Point out every malaria parasite and every leukocyte.
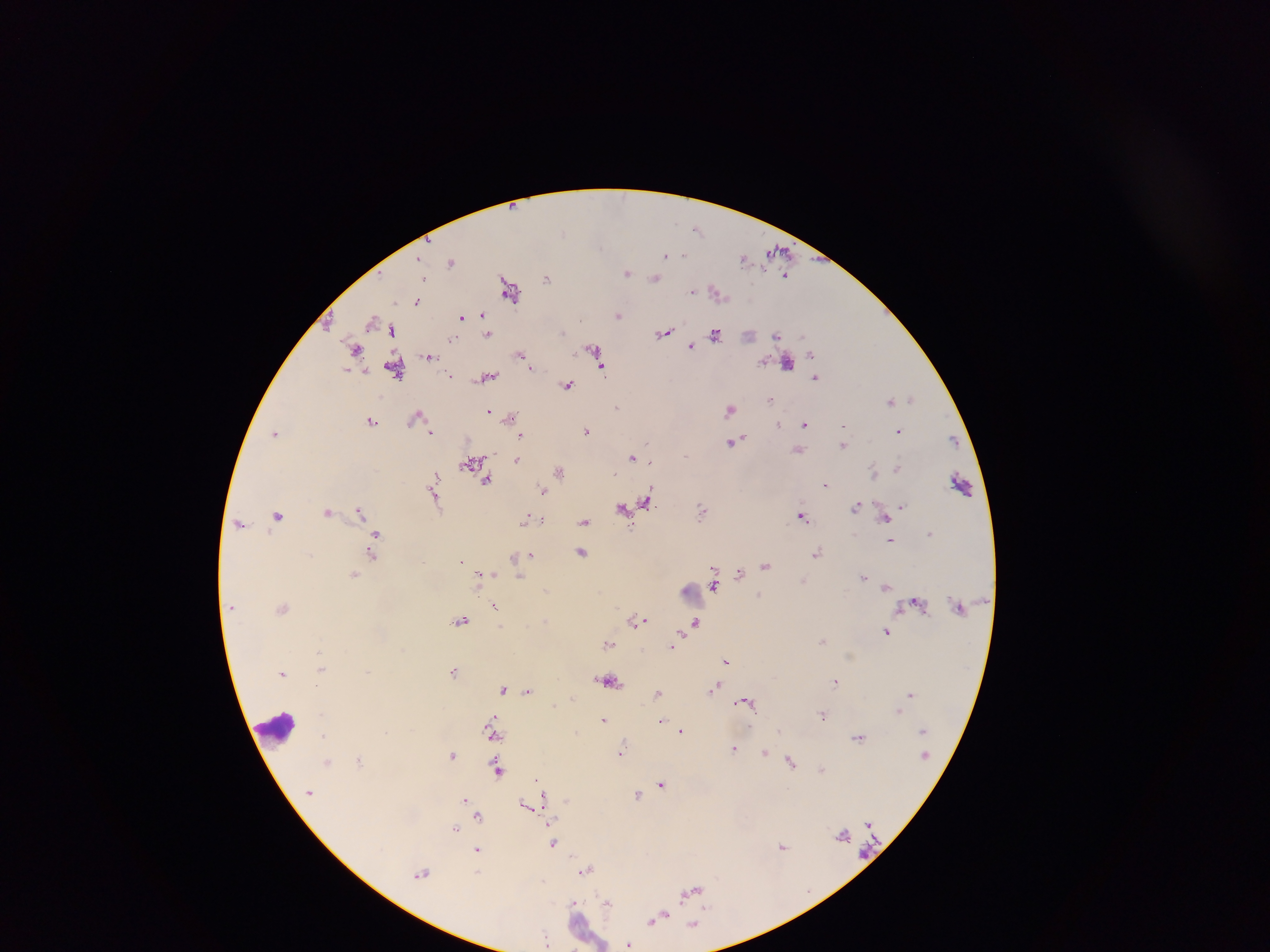

Approximate centers as x y in pixels.
Malaria parasites: 697 228; 564 232; 779 251; 665 255; 683 255; 744 259; 451 262; 627 273; 786 275; 547 278; 655 278; 424 279; 509 289; 693 291; 717 292; 417 301; 619 315; 483 316; 461 317; 372 320; 392 330; 562 332; 488 333; 664 333; 716 334; 776 335; 453 339; 692 346; 355 349; 593 350; 812 354; 521 355; 429 356; 787 362; 600 366; 531 367; 395 369; 452 375; 817 377; 487 378; 567 384; 912 398; 770 399; 890 401; 617 407; 730 410; 489 411; 415 417; 511 417; 371 420; 778 424; 805 424; 843 426; 587 430; 898 431; 431 432; 275 433; 521 436; 733 441; 646 442; 843 444; 800 451; 633 457; 517 458; 474 462; 650 462; 898 467; 873 471; 560 472; 486 480; 825 484; 433 485; 543 490; 435 497; 647 502; 857 506; 903 506; 624 509; 328 510; 702 510; 360 511; 278 515; 801 515; 885 518; 534 519; 525 520; 542 520; 585 521; 240 523; 930 533; 376 535; 891 540; 582 553; 817 553; 372 555; 532 555; 515 557; 461 560; 766 566; 739 573; 482 574; 491 574; 353 575; 863 576; 520 577; 714 585; 886 587; 546 589; 760 595; 495 606; 283 608; 461 620; 638 620; 545 621; 696 623; 887 632; 823 640; 609 643; 672 646; 319 653; 726 660; 321 669; 454 671; 283 673; 608 681; 835 681; 715 688; 504 689; 529 691; 658 693; 910 693; 745 701; 554 705; 897 711; 823 715; 603 719; 662 720; 751 725; 681 731; 492 732; 324 735; 859 737; 734 749; 621 752; 765 753; 452 754; 358 761; 326 762; 791 762; 822 769; 497 770; 538 780; 661 783; 637 795; 542 799; 465 800; 528 805; 478 815; 455 828; 553 843; 783 846; 478 849; 586 870; 422 874; 691 892; 573 904; 608 904; 657 919; 694 925; 546 939; 628 944.
Leukocytes: 694 592; 275 728; 593 934.

image size = 1270×952 pixels
field of view = single
capture = mobile-phone photograph through a microscope
country = Ghana
preparation = thick blood film